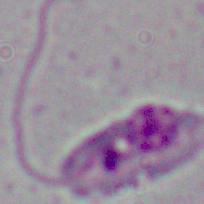
Summary:
  - Magnification: 1000x
  - Identification: Leishmania
  - Modality: micrograph